Classify this cell by malaria status.
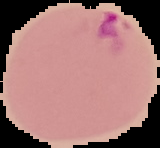

Parasitized.

Summary:
  - Image type: segmented cell region with the area outside set to black
  - Preparation: thin blood film
  - Image size: 160×148 pixels